Outline each uninfected red blood cell.
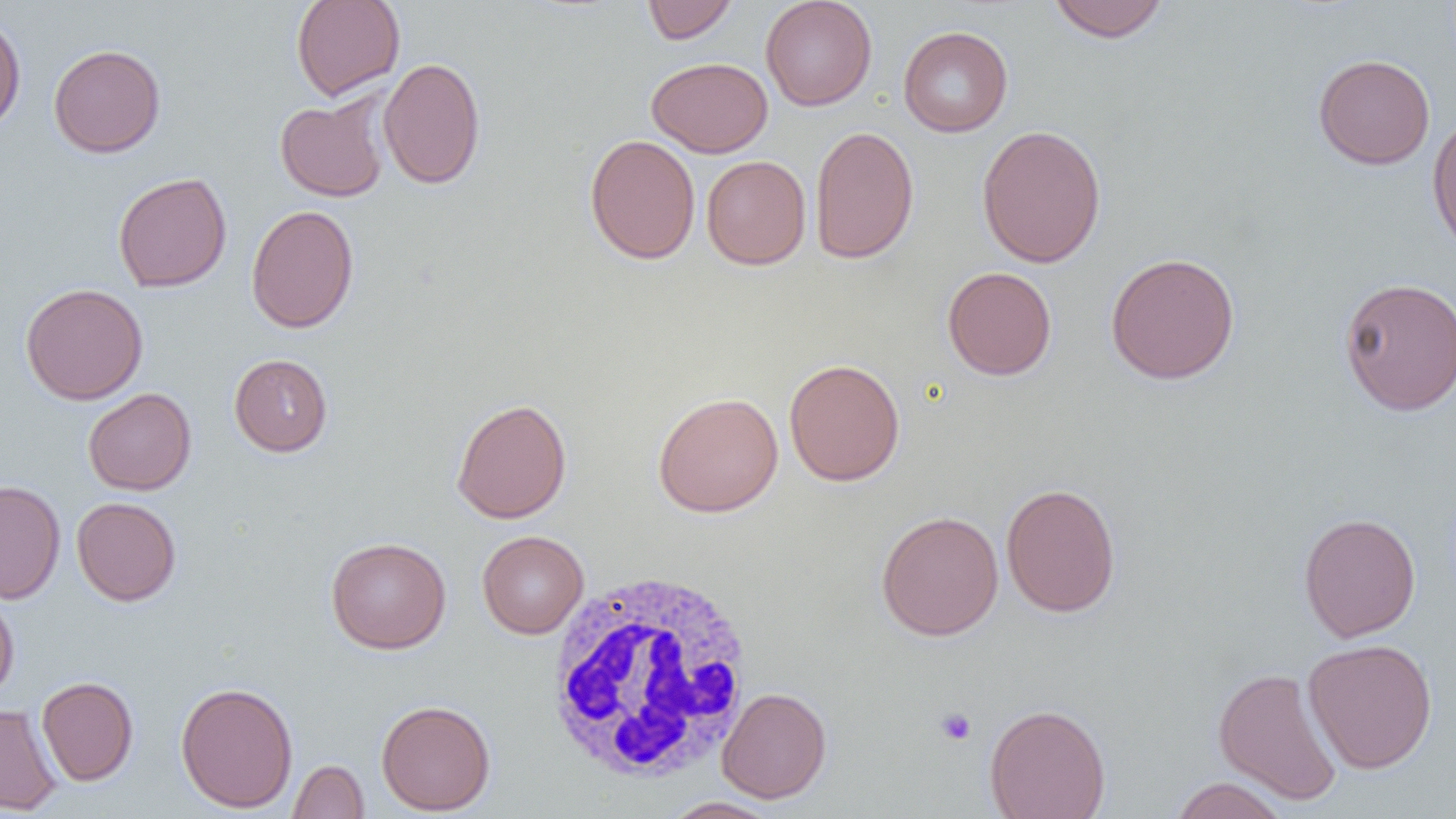

Approximate bounding boxes as (x1,y1)-(x2,y2) corner pairs in pixels.
Uninfected red blood cells: (290,0)-(406,100), (641,0)-(739,44), (760,0)-(877,111), (1047,0)-(1169,43), (0,12)-(27,134), (898,25)-(1013,137), (48,43)-(166,158), (1313,53)-(1435,170), (377,57)-(486,189), (646,57)-(773,157), (275,94)-(390,202), (1427,113)-(1456,256), (810,124)-(920,265), (976,124)-(1107,269), (584,134)-(700,265), (701,155)-(811,270), (113,171)-(232,293), (246,205)-(359,333), (1105,251)-(1240,385), (942,266)-(1057,380), (1338,276)-(1456,416), (20,283)-(148,405), (229,353)-(333,456), (784,358)-(905,486), (83,387)-(197,495), (652,392)-(784,517), (451,397)-(572,524), (0,479)-(66,604), (1001,483)-(1121,617), (71,496)-(182,606), (875,510)-(1004,641), (1298,512)-(1421,642), (477,530)-(589,638), (325,536)-(451,654), (0,591)-(19,701), (1302,638)-(1438,774), (1213,666)-(1343,805), (36,676)-(139,786), (175,680)-(298,813), (716,686)-(832,803), (376,698)-(496,815), (984,702)-(1111,819), (0,704)-(61,814), (288,759)-(369,818), (1168,777)-(1290,819), (661,796)-(782,818).

slide-level diagnosis = no evidence of blood parasites
image size = 1456×819 pixels
modality = optical microscopy
magnification = 1000x
white blood cell locations = approximate bounding boxes as (x1,y1)-(x2,y2) corner pairs in pixels: (541,568)-(759,787)
preparation = thin blood smear
platelet locations = approximate bounding boxes as (x1,y1)-(x2,y2) corner pairs in pixels: (935,707)-(977,746)
field of view = single